Look for parasitized red blood cells.
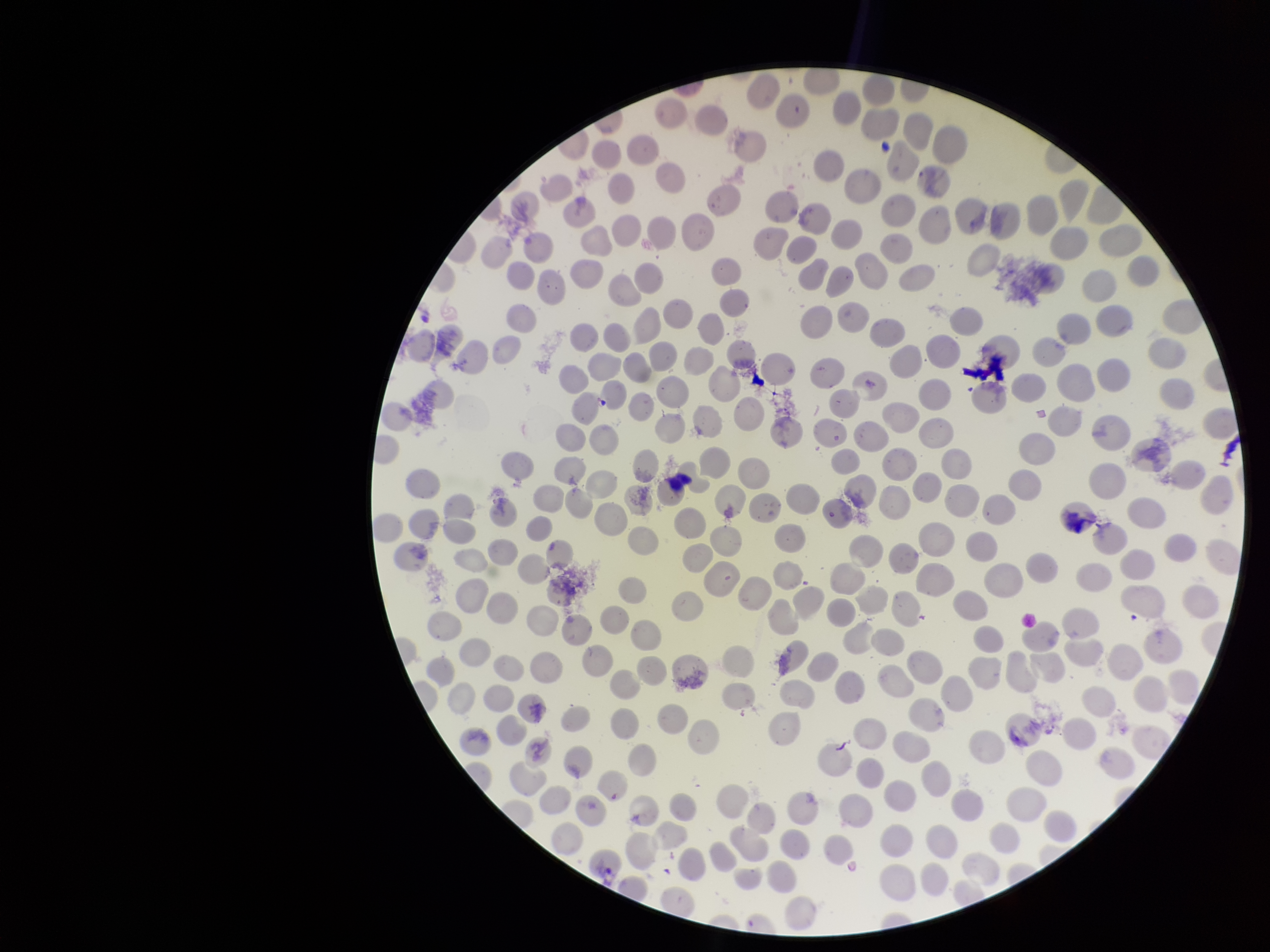
None detected.

red blood cell count = 219
capture = smartphone photograph through the microscope eyepiece
image size = 1270×952 pixels
species reported for this patient = Plasmodium vivax
stain = Giemsa
parasitized red blood cell count = 0
patient malaria status = infected
field of view = single
preparation = thin smear